Comment on the morphology of the red blood cells.
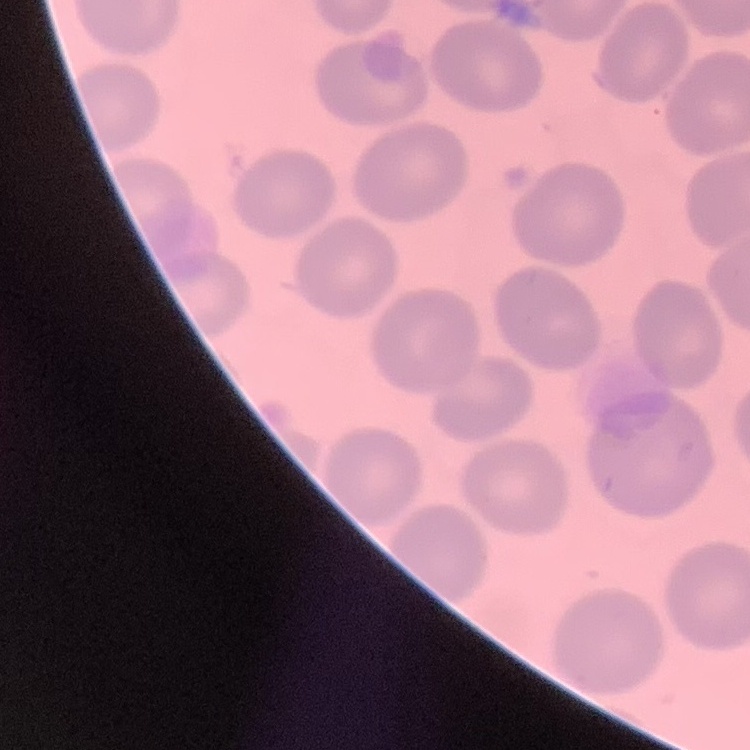

No rouleaux formation.

Square crop of a larger photomicrograph. Field's or Giemsa stain. Thin blood film.